Assess this cell for malaria.
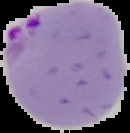

Parasitized.

{
  "preparation": "thin blood smear",
  "image_size": "130×133 pixels",
  "image_type": "segmented cell region with the area outside set to black"
}